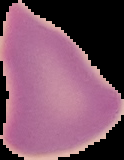

preparation = thin blood film
malaria status = uninfected
image type = cell region segmented out of the field of view; surrounding area masked to black
image size = 124×160 pixels